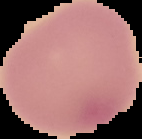 From a thin blood film. Malaria status: uninfected. Segmented cell region on a black background. Image is 142×139 pixels.